Identify the blood parasite species.
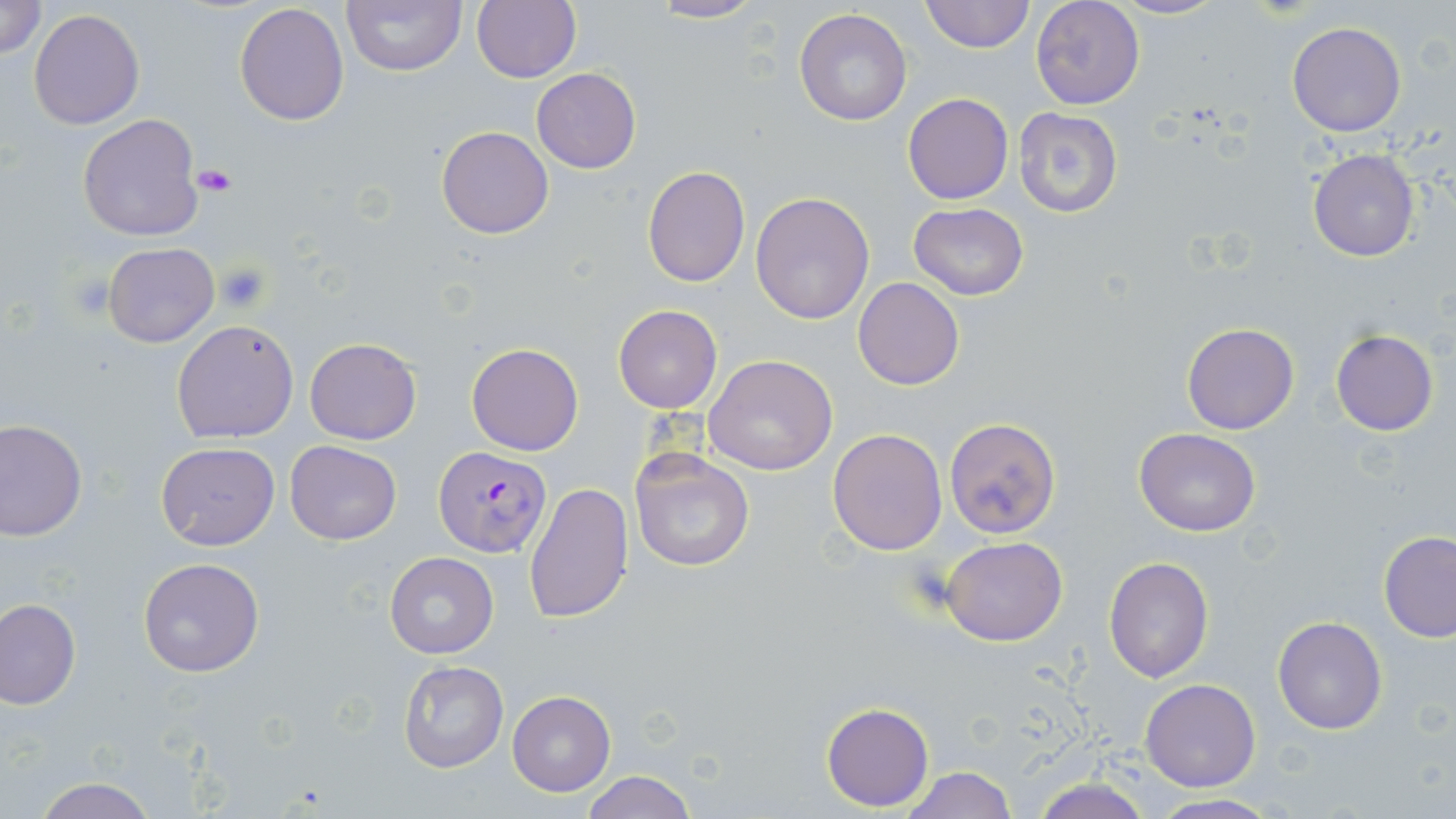

Plasmodium falciparum.

stain: May-Grünwald-Giemsa
plasmodium_falciparum_infected_red_blood_cell_locations: 'approximate bounding boxes as (x1,y1)-(x2,y2) corner pairs in pixels: (431,445)-(549,557)'
image_size: 1456×819 pixels
platelet_locations: 'approximate bounding boxes as (x1,y1)-(x2,y2) corner pairs in pixels: (193,165)-(238,196), (215,261)-(270,311), (67,275)-(115,321)'
modality: optical microscopy
preparation: thin blood smear
magnification: 1000x
field_of_view: single
uninfected_red_blood_cell_locations: 'approximate bounding boxes as (x1,y1)-(x2,y2) corner pairs in pixels: (0,0)-(47,59), (343,0)-(466,75), (471,0)-(581,85), (642,0)-(768,24), (921,0)-(1034,53), (1031,0)-(1144,110), (1111,0)-(1227,20), (234,3)-(349,126), (29,9)-(144,129), (793,9)-(913,127), (1285,22)-(1407,137), (532,67)-(640,174), (903,92)-(1013,204), (1013,108)-(1123,218), (78,112)-(205,241), (436,126)-(554,240), (1308,148)-(1421,262), (641,166)-(750,288), (749,191)-(875,325), (907,203)-(1032,302), (103,242)-(219,347), (853,276)-(965,391), (612,305)-(723,413), (172,318)-(300,443), (1182,322)-(1298,435), (1331,330)-(1438,437), (305,337)-(421,444), (467,343)-(583,457), (705,353)-(839,476), (944,417)-(1064,540), (0,418)-(87,540), (828,427)-(946,555), (1134,428)-(1260,536), (284,440)-(402,545), (154,442)-(280,551), (629,445)-(756,572), (523,482)-(632,626), (1378,531)-(1456,641), (941,536)-(1068,646), (384,551)-(498,658), (1103,556)-(1213,682), (138,557)-(266,677), (1,599)-(80,708), (1272,616)-(1389,735), (399,659)-(508,773), (1141,678)-(1262,791), (507,690)-(615,796), (821,702)-(934,812), (897,764)-(1016,819), (579,771)-(699,819), (1026,776)-(1156,819), (30,777)-(160,819), (1144,794)-(1284,818)'